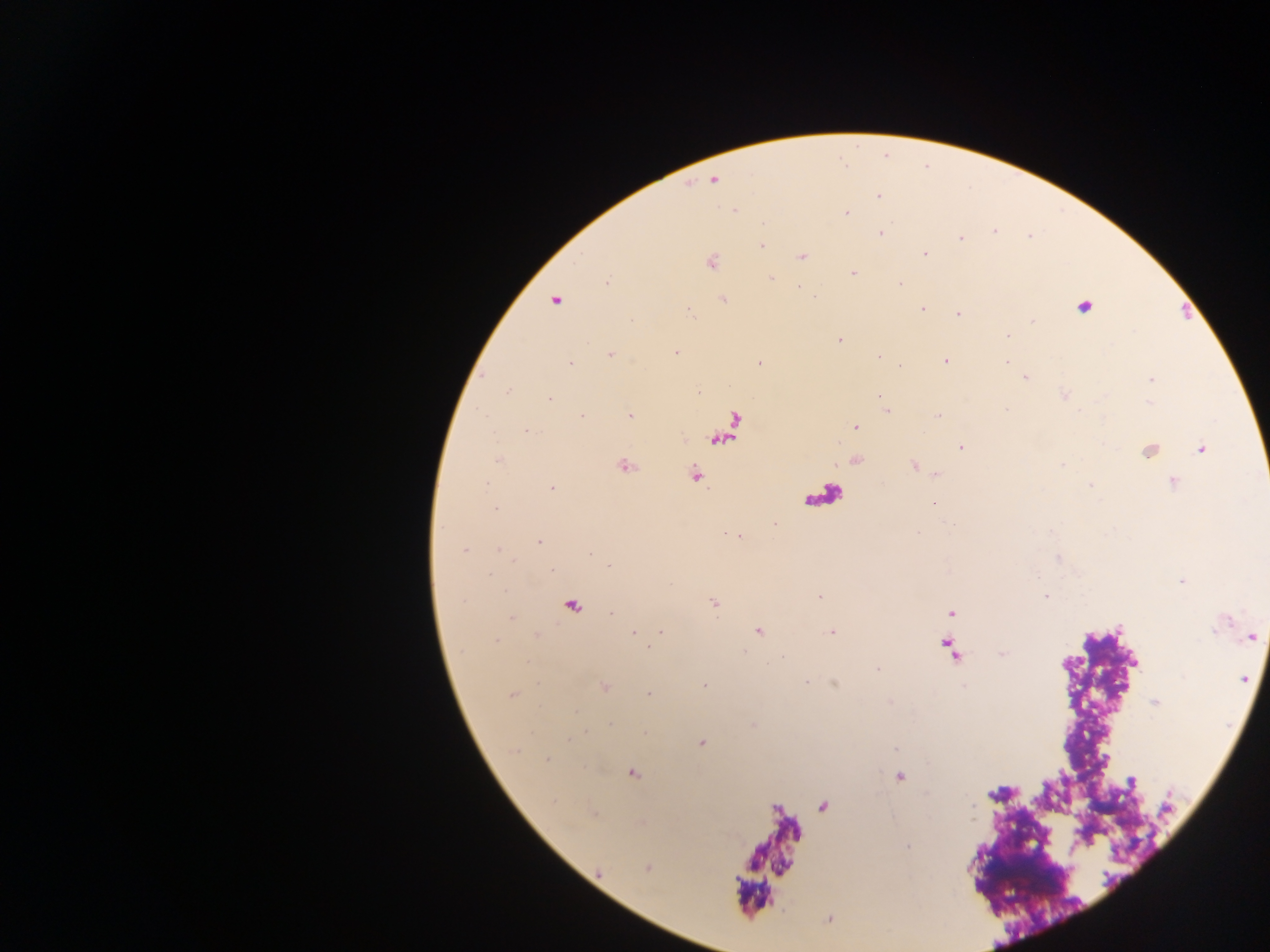
Approximate centers as {x, y} in pixels.
Summary:
  - Leukocyte locations: {822, 491}
  - Malaria parasite locations: {714, 180}, {878, 195}, {734, 211}, {846, 213}, {763, 223}, {994, 231}, {882, 233}, {960, 238}, {762, 246}, {925, 254}, {802, 257}, {712, 262}, {853, 273}, {771, 278}, {607, 280}, {900, 284}, {723, 299}, {555, 300}, {1083, 307}, {921, 309}, {690, 313}, {958, 314}, {1033, 321}, {1007, 335}, {840, 340}, {675, 353}, {610, 354}, {879, 356}, {945, 361}, {1006, 362}, {570, 363}, {760, 363}, {899, 366}, {1026, 377}, {1152, 379}, {508, 391}, {697, 393}, {880, 396}, {549, 398}, {884, 409}, {1007, 410}, {581, 415}, {629, 415}, {938, 416}, {855, 427}, {527, 430}, {729, 430}, {961, 447}, {1201, 449}, {1149, 451}, {498, 460}, {914, 465}, {625, 466}, {1061, 466}, {936, 474}, {695, 475}, {1173, 482}, {1090, 485}, {552, 488}, {934, 503}, {495, 509}, {774, 524}, {919, 532}, {539, 541}, {464, 549}, {499, 549}, {1059, 558}, {608, 566}, {552, 571}, {1182, 581}, {820, 596}, {1046, 596}, {714, 604}, {573, 605}, {951, 612}, {612, 613}, {511, 617}, {758, 631}, {661, 632}, {634, 633}, {831, 633}, {536, 635}, {1252, 636}, {496, 641}, {783, 657}, {1243, 679}, {806, 682}, {704, 686}, {605, 687}, {648, 694}, {512, 696}, {1155, 702}, {611, 723}, {701, 743}, {895, 748}, {547, 760}, {632, 773}, {901, 776}, {1132, 782}, {908, 846}
  - Field of view: single
  - Country: Ghana
  - Image size: 1270×952 pixels
  - Capture: mobile-phone photograph through a microscope
  - Preparation: thick blood film